Evaluate for Plasmodium parasites.
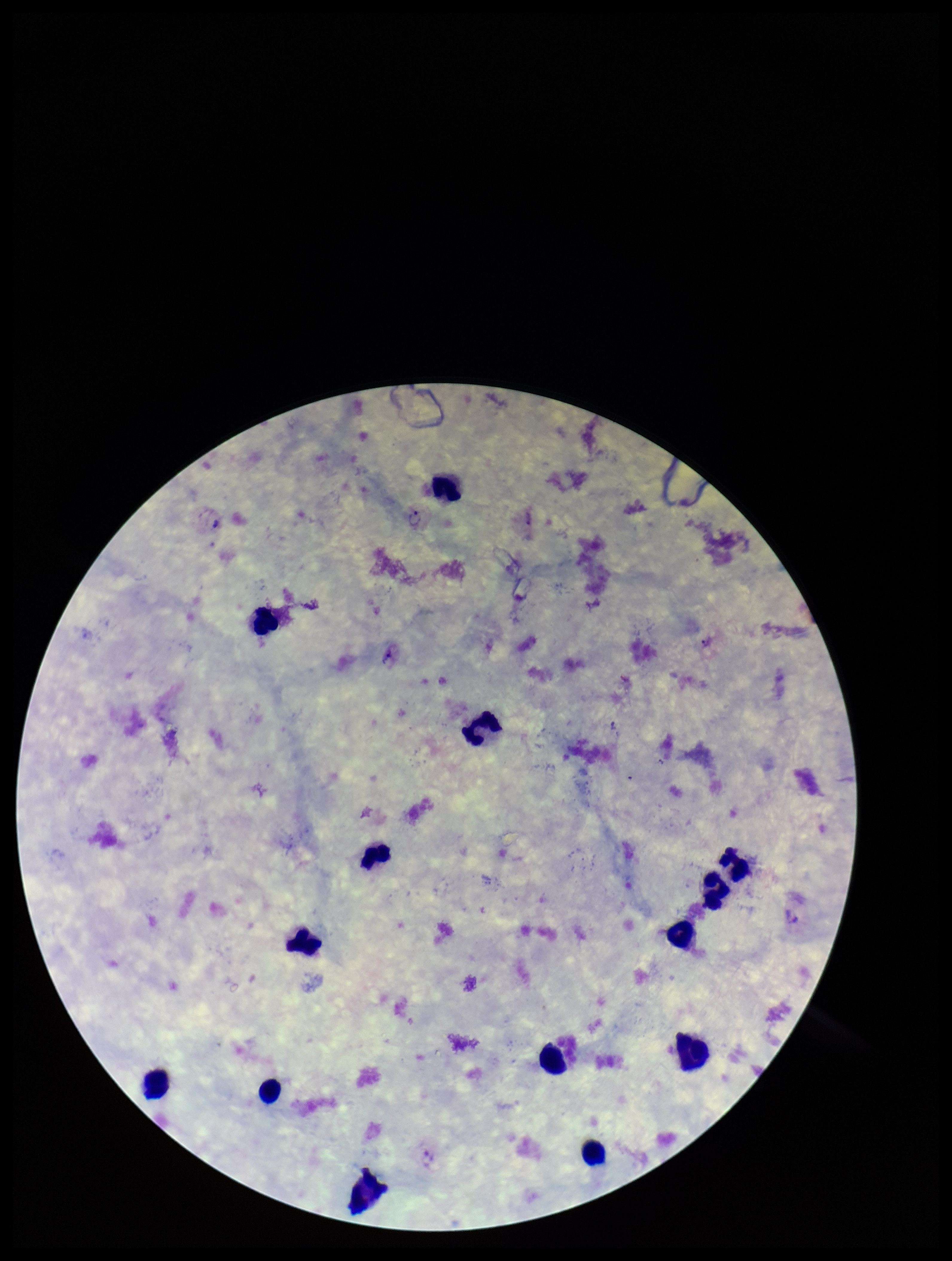

Seen.

Patient malaria status: infected. Giemsa stain. Leukocyte count: 12. Preparation: thick blood smear. Image is 952×1261 pixels. Photographed through the microscope eyepiece with a smartphone camera. One field from this slide. Parasite count: 2. Species reported for this patient: Plasmodium vivax.